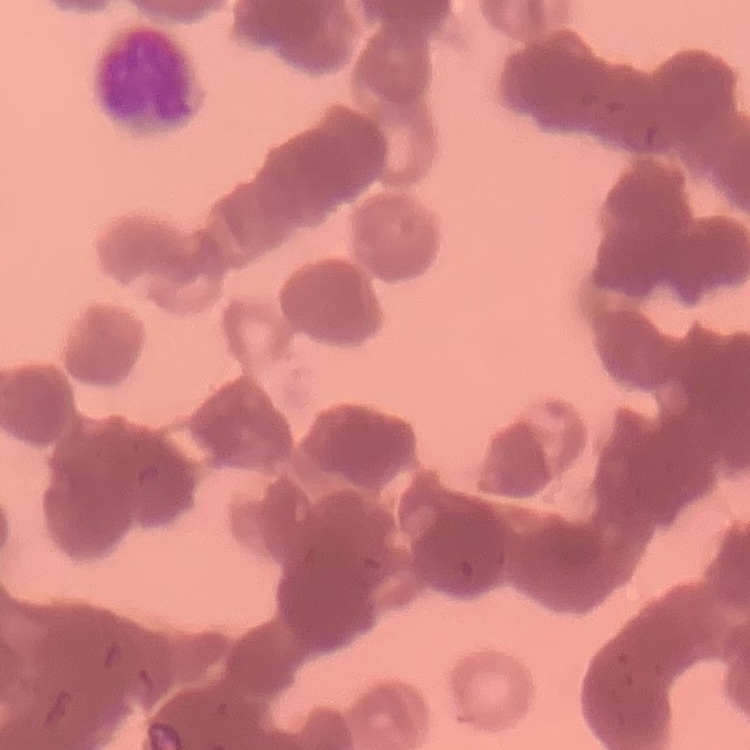

Summary:
  - Red blood cell morphology: rouleaux formation
  - Stain: Field's or Giemsa
  - Preparation: thin blood film
  - Image type: one tile cut from a larger photomicrograph